Locate every Plasmodium falciparum-infected red blood cell.
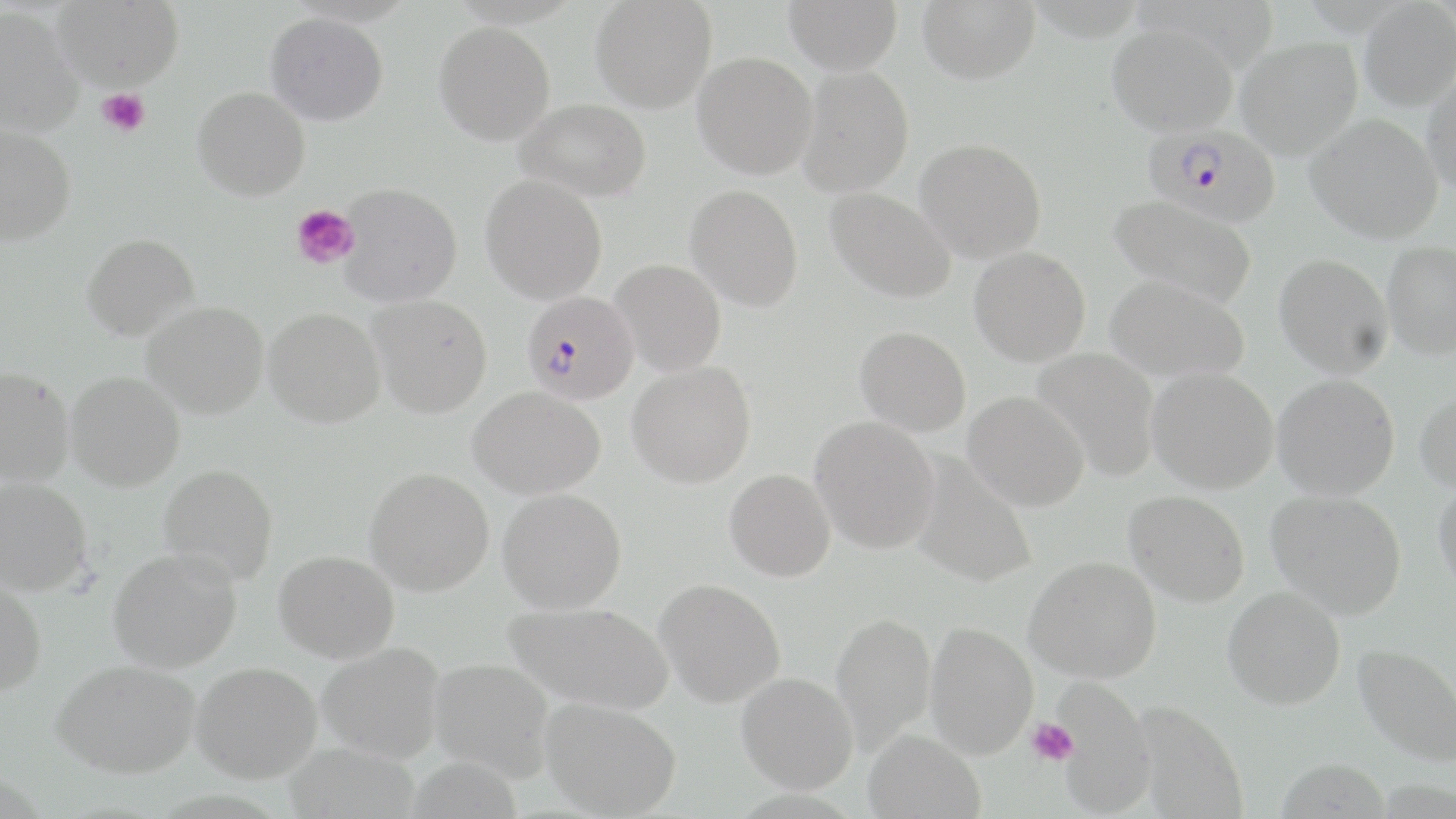
Approximate bounding boxes as (x1, y1, x2, y2) in pixels.
Plasmodium falciparum-infected red blood cells: (1143, 125, 1281, 226), (522, 291, 639, 404).

Uninfected red blood cell locations: (51, 0, 184, 91), (590, 0, 717, 113), (784, 0, 903, 75), (917, 0, 1040, 84), (1358, 2, 1456, 112), (0, 6, 85, 138), (265, 12, 388, 126), (434, 22, 555, 146), (1107, 22, 1239, 137), (1236, 37, 1363, 160), (692, 52, 818, 179), (796, 64, 914, 197), (1422, 65, 1456, 197), (192, 86, 310, 201), (516, 98, 651, 201), (1305, 113, 1444, 244), (0, 126, 76, 245), (915, 138, 1046, 263), (480, 174, 607, 305), (338, 183, 463, 307), (685, 184, 804, 312), (826, 188, 956, 304), (1108, 194, 1258, 310), (81, 233, 200, 341), (1382, 242, 1456, 359), (969, 246, 1091, 366), (1274, 253, 1393, 378), (610, 259, 726, 376), (1104, 275, 1250, 383), (369, 295, 493, 418), (142, 301, 269, 419), (263, 307, 386, 428), (855, 326, 971, 436), (1031, 347, 1162, 482), (627, 361, 756, 489), (1147, 366, 1278, 493), (1, 367, 75, 486), (66, 371, 185, 491), (1273, 374, 1400, 499), (468, 386, 606, 499), (1414, 389, 1456, 494), (963, 391, 1090, 512), (809, 416, 940, 554), (911, 453, 1037, 589), (158, 464, 279, 586), (365, 467, 495, 596), (724, 469, 836, 582), (0, 477, 92, 597), (1433, 480, 1456, 598), (497, 489, 627, 613), (1124, 490, 1250, 606), (1266, 490, 1407, 619), (108, 548, 242, 673), (274, 550, 400, 663), (1025, 556, 1161, 683), (0, 577, 47, 698), (655, 579, 786, 707), (1223, 587, 1345, 709), (504, 601, 675, 715), (831, 612, 937, 754), (925, 622, 1039, 758), (318, 643, 445, 763), (1353, 644, 1456, 768), (429, 657, 554, 782), (52, 659, 200, 778), (190, 661, 321, 784), (736, 672, 858, 794), (1052, 679, 1156, 817), (540, 697, 682, 818), (1133, 701, 1248, 819), (863, 729, 985, 819), (284, 741, 419, 818), (1276, 756, 1394, 818). Platelet locations: (97, 89, 150, 137), (291, 204, 360, 269), (1026, 717, 1079, 767). Slide-level diagnosis: Plasmodium falciparum. Image is 1456×819 pixels. Thin blood smear. Captured at 1000x magnification. May-Grünwald-Giemsa stain. Light microscopy. One field of a larger specimen.